Locate every blood parasite and identify its species.
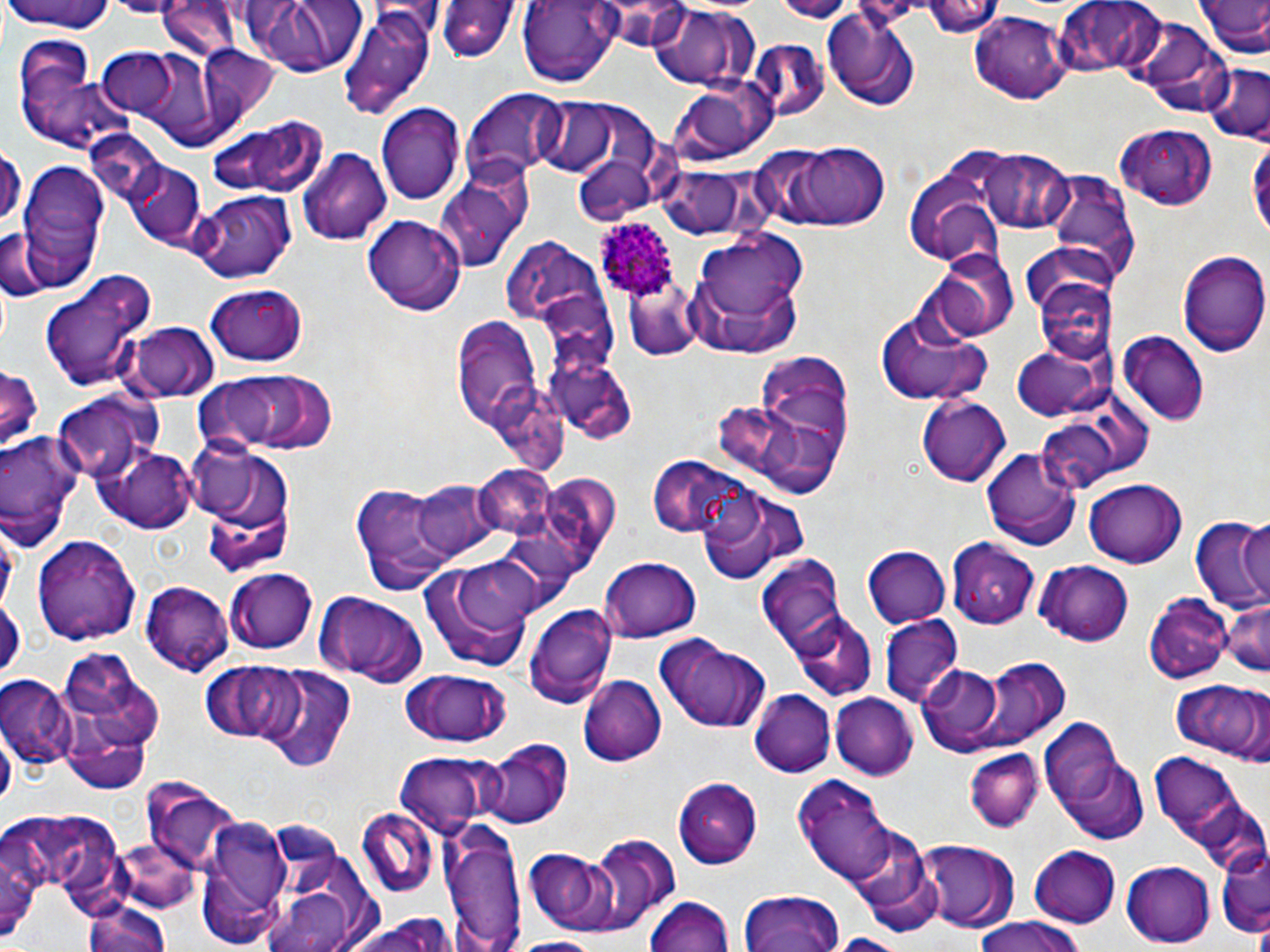

Approximate bounding boxes as named x1/y1/x2/y2 corners in pixels.
Plasmodium ovale-infected red blood cells: (x1=592, y1=218, x2=682, y2=300).
No Plasmodium falciparum, Plasmodium malariae, Plasmodium vivax, Babesia divergens, or Trypanosoma brucei observed.

Uninfected red blood cell locations: (x1=253, y1=0, x2=361, y2=78), (x1=518, y1=0, x2=616, y2=86), (x1=922, y1=0, x2=1005, y2=43), (x1=1053, y1=0, x2=1169, y2=80), (x1=1197, y1=0, x2=1269, y2=63), (x1=3, y1=1, x2=118, y2=36), (x1=432, y1=1, x2=521, y2=63), (x1=157, y1=2, x2=240, y2=64), (x1=341, y1=5, x2=437, y2=118), (x1=649, y1=6, x2=756, y2=91), (x1=821, y1=8, x2=922, y2=111), (x1=970, y1=11, x2=1067, y2=103), (x1=1124, y1=15, x2=1231, y2=117), (x1=11, y1=36, x2=126, y2=153), (x1=744, y1=40, x2=829, y2=123), (x1=194, y1=45, x2=281, y2=134), (x1=98, y1=50, x2=178, y2=120), (x1=1202, y1=63, x2=1269, y2=144), (x1=670, y1=79, x2=774, y2=161), (x1=463, y1=90, x2=564, y2=184), (x1=530, y1=100, x2=620, y2=176), (x1=377, y1=103, x2=464, y2=206), (x1=210, y1=117, x2=327, y2=198), (x1=1113, y1=123, x2=1219, y2=211), (x1=761, y1=139, x2=896, y2=233), (x1=1248, y1=140, x2=1269, y2=248), (x1=0, y1=143, x2=23, y2=234), (x1=298, y1=148, x2=392, y2=245), (x1=978, y1=148, x2=1074, y2=232), (x1=571, y1=151, x2=660, y2=227), (x1=123, y1=159, x2=207, y2=248), (x1=15, y1=163, x2=111, y2=289), (x1=434, y1=166, x2=532, y2=274), (x1=654, y1=166, x2=752, y2=238), (x1=1044, y1=167, x2=1139, y2=287), (x1=906, y1=169, x2=1006, y2=266), (x1=190, y1=190, x2=297, y2=281), (x1=363, y1=215, x2=463, y2=315), (x1=0, y1=227, x2=45, y2=303), (x1=682, y1=232, x2=811, y2=356), (x1=498, y1=235, x2=593, y2=318), (x1=1020, y1=243, x2=1119, y2=322), (x1=1177, y1=248, x2=1270, y2=357), (x1=933, y1=250, x2=1019, y2=342), (x1=38, y1=269, x2=157, y2=393), (x1=1033, y1=277, x2=1115, y2=367), (x1=0, y1=283, x2=12, y2=352), (x1=205, y1=283, x2=310, y2=366), (x1=626, y1=286, x2=712, y2=366), (x1=875, y1=306, x2=995, y2=408), (x1=452, y1=320, x2=546, y2=433), (x1=126, y1=323, x2=219, y2=402), (x1=1117, y1=331, x2=1211, y2=424), (x1=1011, y1=343, x2=1109, y2=421), (x1=744, y1=354, x2=854, y2=488), (x1=557, y1=360, x2=639, y2=441), (x1=0, y1=366, x2=44, y2=449), (x1=199, y1=370, x2=338, y2=456), (x1=51, y1=389, x2=159, y2=485), (x1=917, y1=395, x2=1011, y2=487), (x1=1035, y1=417, x2=1123, y2=492), (x1=0, y1=431, x2=85, y2=549), (x1=981, y1=447, x2=1081, y2=551), (x1=97, y1=448, x2=199, y2=533), (x1=195, y1=450, x2=297, y2=577), (x1=649, y1=457, x2=756, y2=540), (x1=470, y1=465, x2=561, y2=540), (x1=548, y1=474, x2=617, y2=559), (x1=1085, y1=475, x2=1185, y2=564), (x1=412, y1=480, x2=499, y2=560), (x1=351, y1=483, x2=460, y2=595), (x1=700, y1=488, x2=811, y2=584), (x1=1238, y1=517, x2=1269, y2=605), (x1=1191, y1=520, x2=1270, y2=616), (x1=33, y1=532, x2=140, y2=643), (x1=947, y1=540, x2=1039, y2=626), (x1=863, y1=546, x2=950, y2=627), (x1=759, y1=553, x2=850, y2=661), (x1=418, y1=557, x2=539, y2=675), (x1=598, y1=557, x2=703, y2=642), (x1=1034, y1=562, x2=1134, y2=646), (x1=226, y1=568, x2=321, y2=653), (x1=141, y1=581, x2=234, y2=676), (x1=313, y1=591, x2=428, y2=688), (x1=1147, y1=591, x2=1232, y2=683), (x1=0, y1=593, x2=23, y2=685), (x1=1220, y1=594, x2=1270, y2=676), (x1=524, y1=602, x2=616, y2=709), (x1=879, y1=615, x2=962, y2=708), (x1=789, y1=616, x2=877, y2=702), (x1=652, y1=635, x2=772, y2=735), (x1=61, y1=650, x2=163, y2=770), (x1=977, y1=660, x2=1068, y2=746), (x1=214, y1=663, x2=311, y2=746), (x1=922, y1=666, x2=1005, y2=753), (x1=258, y1=667, x2=357, y2=771), (x1=401, y1=671, x2=509, y2=748), (x1=1, y1=673, x2=75, y2=769), (x1=580, y1=676, x2=666, y2=768), (x1=1172, y1=677, x2=1269, y2=764), (x1=748, y1=689, x2=837, y2=779), (x1=832, y1=694, x2=917, y2=779), (x1=62, y1=711, x2=151, y2=797), (x1=1040, y1=720, x2=1128, y2=816), (x1=478, y1=738, x2=572, y2=828), (x1=1149, y1=746, x2=1261, y2=870), (x1=965, y1=747, x2=1045, y2=832), (x1=391, y1=752, x2=499, y2=838), (x1=1058, y1=755, x2=1150, y2=844), (x1=792, y1=775, x2=900, y2=889), (x1=675, y1=779, x2=763, y2=866), (x1=149, y1=789, x2=244, y2=879), (x1=9, y1=808, x2=130, y2=914), (x1=355, y1=810, x2=440, y2=896), (x1=268, y1=816, x2=344, y2=895), (x1=197, y1=817, x2=291, y2=943), (x1=441, y1=818, x2=526, y2=952), (x1=1, y1=823, x2=45, y2=947), (x1=847, y1=824, x2=937, y2=911), (x1=585, y1=835, x2=679, y2=933), (x1=916, y1=841, x2=1020, y2=933), (x1=1216, y1=844, x2=1268, y2=939), (x1=1027, y1=845, x2=1122, y2=927), (x1=525, y1=847, x2=616, y2=934), (x1=1121, y1=860, x2=1214, y2=947), (x1=740, y1=888, x2=844, y2=952), (x1=645, y1=895, x2=736, y2=952), (x1=262, y1=896, x2=358, y2=951), (x1=83, y1=899, x2=173, y2=952), (x1=344, y1=914, x2=460, y2=952), (x1=972, y1=919, x2=1086, y2=952), (x1=824, y1=934, x2=914, y2=952), (x1=509, y1=937, x2=607, y2=952). Slide-level diagnosis: Plasmodium ovale. May-Grünwald-Giemsa stain. Captured at 1000x magnification. Thin blood smear. Optical microscopy. Image is 1270×952 pixels. Single field of view.